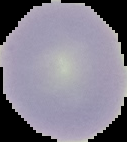

Summary:
  - Preparation: thin blood smear
  - Result: negative for Plasmodium parasites
  - Image type: segmented cell region with the area outside set to black
  - Image size: 127×142 pixels